Report the malaria status.
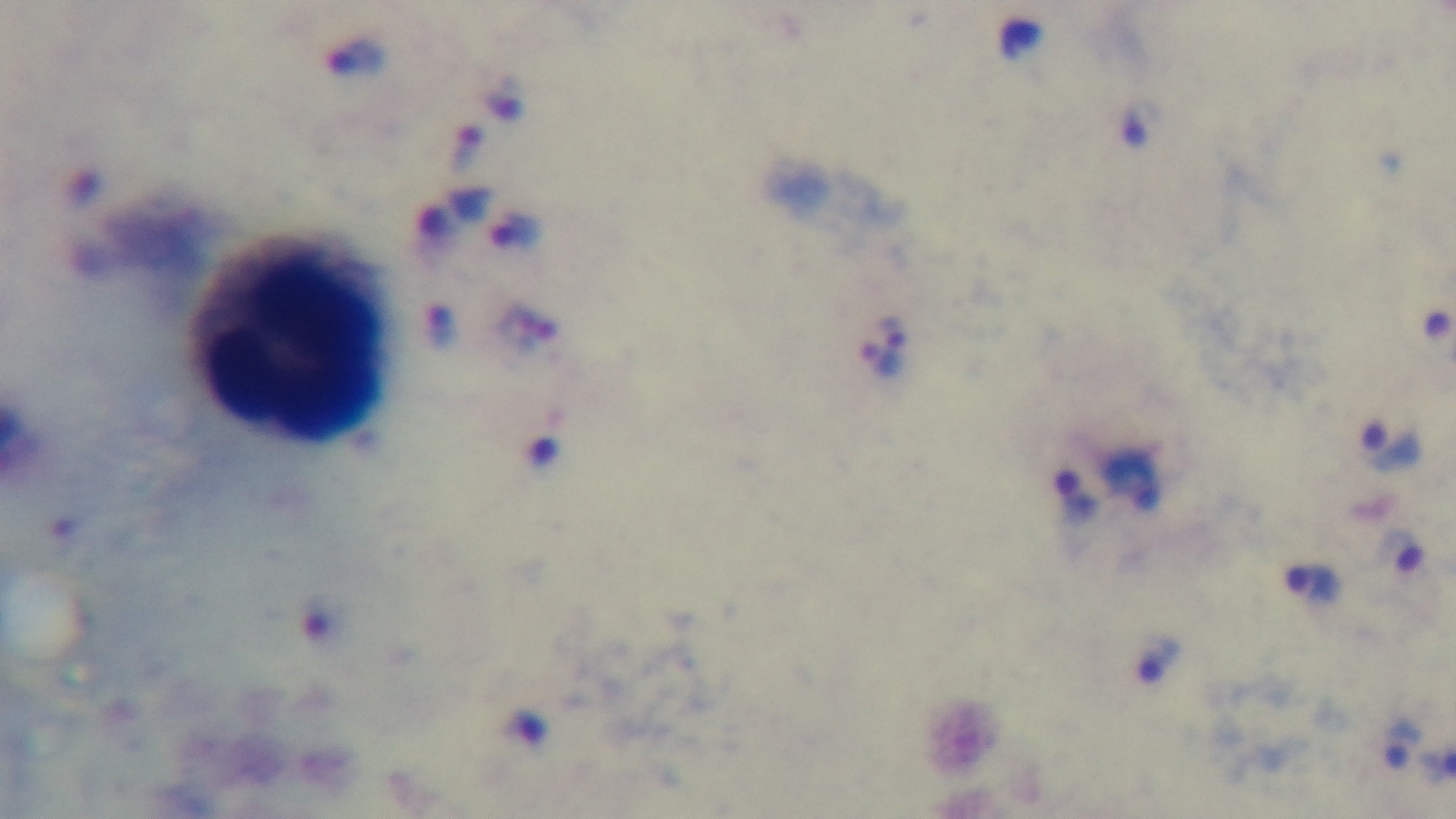
Infected.

One field from the slide. Captured with a mounted 4K digital camera. Preparation: thick smear. 100x oil-immersion objective. Photomicrograph. Giemsa-stained.